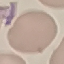 Malaria status: uninfected. Automatically extracted cell patch, resized to 64 × 64 pixels. Giemsa-stained preparation. Acquired by smartphone through the microscope eyepiece. Thin smear of blood.